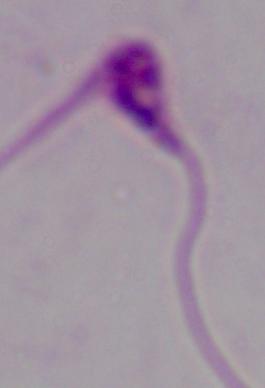
Captured at 1000x magnification. A Leishmania parasite is seen. Micrograph.